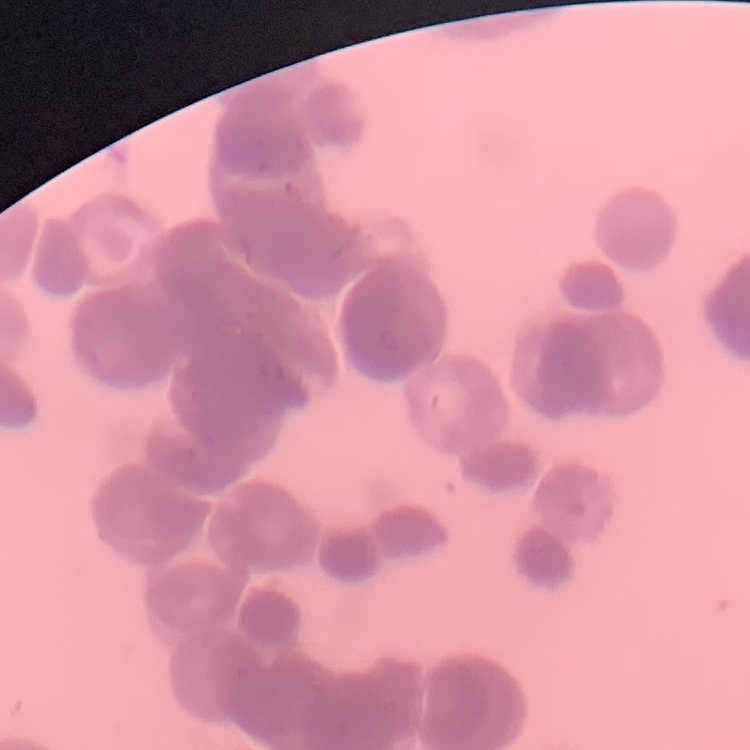
Summary:
  - Red blood cell morphology: rouleaux formation
  - Preparation: thin blood smear
  - Image type: square crop of a larger photomicrograph
  - Stain: Field's or Giemsa